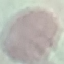
Summary:
  - Result: no malaria parasites seen
  - Capture: smartphone camera at the microscope eyepiece
  - Stain: Giemsa
  - Image type: automatically extracted cell patch, resized to 64 × 64 pixels
  - Preparation: thin blood film